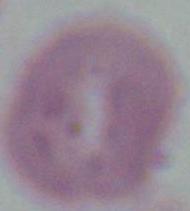

Photomicrograph. 1000x magnification. A red blood cell is shown.